Classify this cell by malaria status.
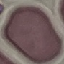
Uninfected.

Thin blood film. Automatically extracted cell patch, resized to 64 × 64 pixels. Giemsa stain. Acquired by smartphone through the microscope eyepiece.